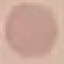
Summary:
  - Result: negative for malaria parasites
  - Preparation: thin blood film
  - Image type: automatically extracted cell patch, resized to 64 × 64 pixels
  - Capture: smartphone through the microscope eyepiece
  - Stain: Giemsa